Name the blood parasite species.
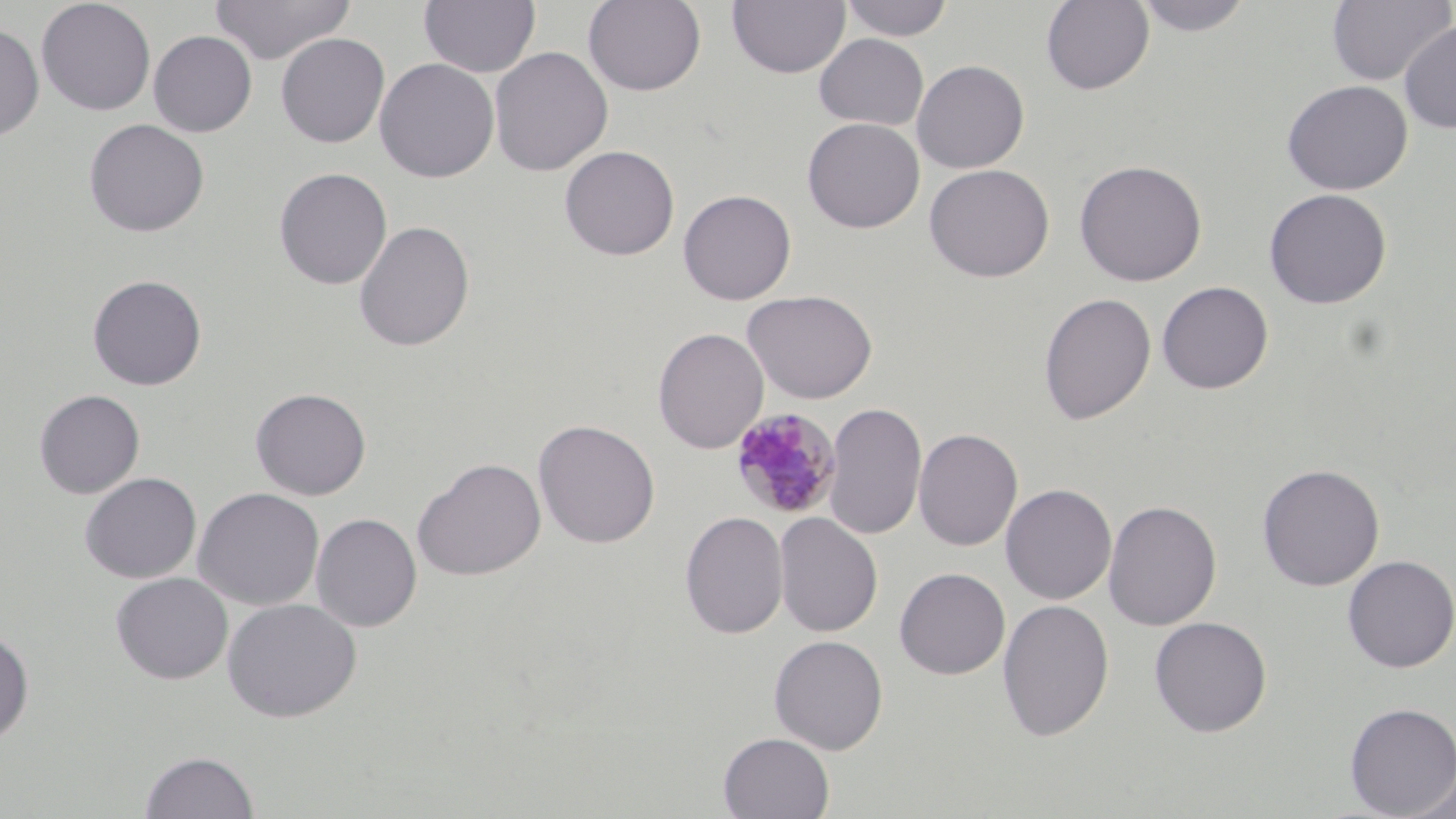

Plasmodium malariae.

Summary:
  - Coordinate format: approximate bounding boxes as (x1,y1)-(x2,y2) corner pairs in pixels
  - Plasmodium malariae-infected red blood cell locations: (730,408)-(842,520)
  - Uninfected red blood cell locations: (36,0)-(156,116), (211,0)-(354,64), (419,0)-(541,78), (583,0)-(707,96), (728,0)-(850,79), (840,0)-(953,42), (1040,0)-(1154,95), (1132,0)-(1255,37), (1327,0)-(1454,86), (1398,21)-(1456,134), (0,23)-(44,142), (148,30)-(257,136), (276,33)-(390,147), (814,33)-(929,130), (489,46)-(613,177), (374,58)-(499,183), (912,59)-(1029,174), (1281,80)-(1413,195), (802,117)-(925,233), (83,118)-(209,237), (559,145)-(680,261), (1074,159)-(1207,287), (924,163)-(1055,282), (274,168)-(392,290), (1264,188)-(1392,309), (678,189)-(797,305), (354,221)-(475,352), (87,274)-(207,391), (1157,281)-(1274,394), (742,289)-(878,404), (1038,293)-(1156,425), (652,327)-(769,454), (250,387)-(371,500), (34,389)-(145,498), (824,401)-(927,541), (533,419)-(660,548), (913,427)-(1023,551), (413,457)-(546,581), (1257,463)-(1385,591), (79,472)-(201,583), (1000,483)-(1117,604), (192,487)-(325,610), (1103,499)-(1222,631), (679,511)-(789,639), (312,512)-(422,632), (773,512)-(883,637), (1341,554)-(1456,673), (894,567)-(1010,679), (110,571)-(232,684), (221,597)-(362,723), (997,597)-(1115,743), (1149,616)-(1272,737), (0,627)-(34,745), (769,634)-(889,754), (1344,701)-(1456,817), (717,732)-(835,818), (139,750)-(259,818), (1404,766)-(1456,818)
  - Magnification: 1000x
  - Modality: light microscopy
  - Image size: 1456×819 pixels
  - Stain: May-Grünwald-Giemsa
  - Preparation: thin blood smear
  - Field of view: single